State which parasite is depicted.
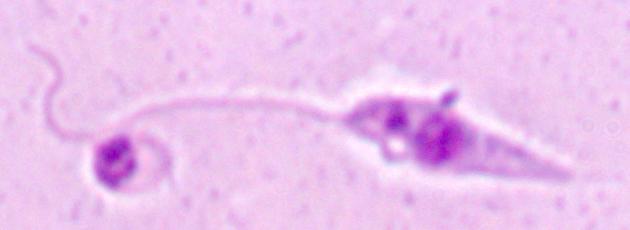

This is Leishmania.

Micrograph. Captured at 1000x magnification.